Identify the blood parasite species.
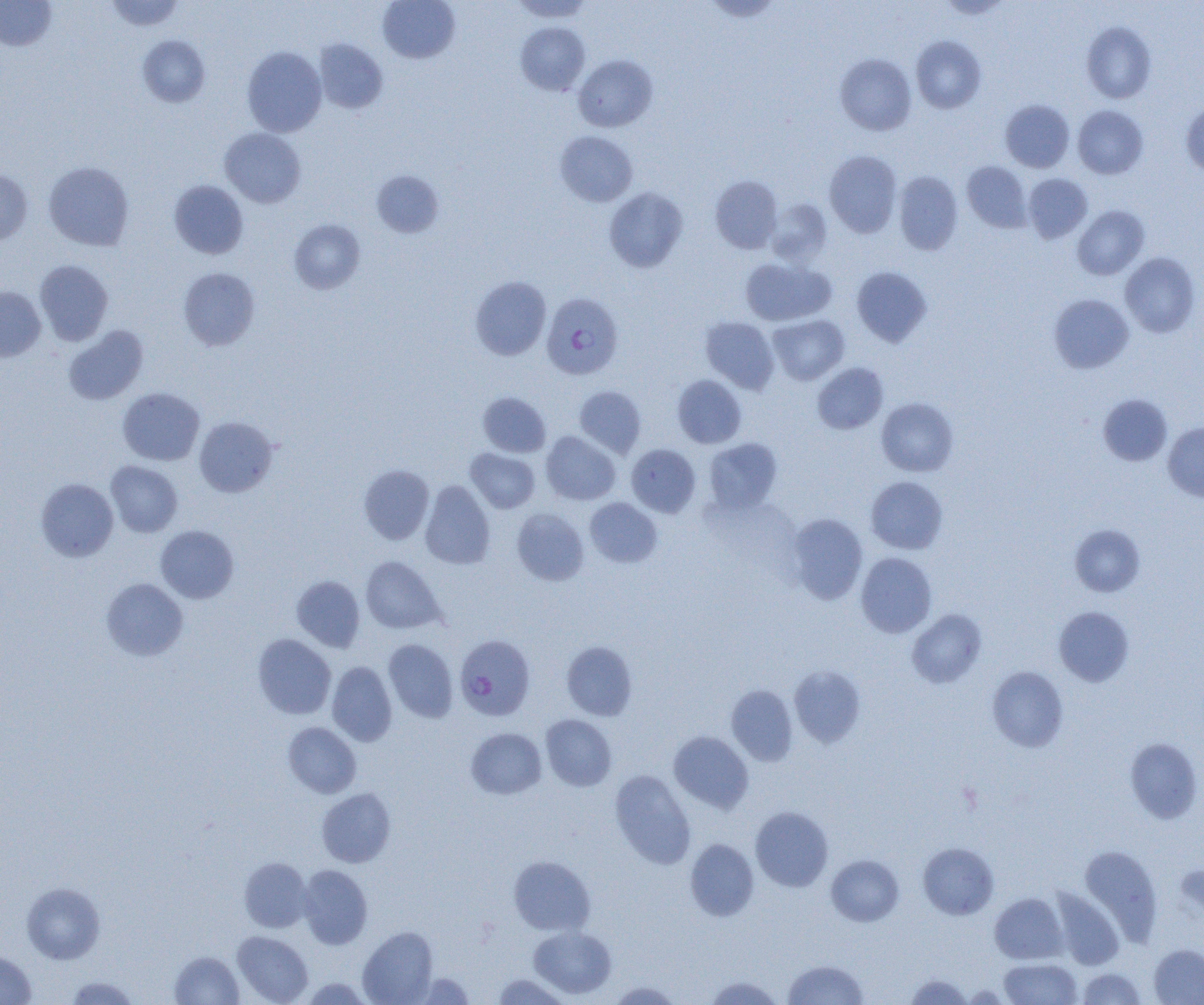

Plasmodium falciparum.

magnification = 1000x
Plasmodium falciparum-infected red blood cell locations = approximate bounding boxes as named x1/y1/x2/y2 corners in pixels: (x1=542, y1=292, x2=623, y2=379), (x1=455, y1=635, x2=535, y2=721)
preparation = thin blood smear
field of view = one of a larger specimen
modality = optical microscopy
image size = 1204×1005 pixels
uninfected red blood cell locations = approximate bounding boxes as named x1/y1/x2/y2 corners in pixels: (x1=0, y1=0, x2=56, y2=51), (x1=105, y1=0, x2=185, y2=31), (x1=378, y1=0, x2=460, y2=63), (x1=509, y1=0, x2=595, y2=22), (x1=938, y1=0, x2=1012, y2=19), (x1=1081, y1=21, x2=1156, y2=103), (x1=515, y1=22, x2=590, y2=95), (x1=138, y1=35, x2=210, y2=107), (x1=911, y1=35, x2=986, y2=114), (x1=314, y1=39, x2=388, y2=114), (x1=242, y1=46, x2=327, y2=137), (x1=835, y1=53, x2=916, y2=136), (x1=573, y1=54, x2=658, y2=132), (x1=1000, y1=99, x2=1074, y2=172), (x1=1181, y1=101, x2=1204, y2=177), (x1=1073, y1=105, x2=1148, y2=179), (x1=219, y1=127, x2=306, y2=208), (x1=555, y1=131, x2=638, y2=207), (x1=824, y1=150, x2=902, y2=237), (x1=962, y1=161, x2=1031, y2=233), (x1=43, y1=162, x2=134, y2=251), (x1=0, y1=169, x2=33, y2=245), (x1=372, y1=170, x2=444, y2=238), (x1=894, y1=171, x2=963, y2=255), (x1=1023, y1=173, x2=1093, y2=243), (x1=710, y1=175, x2=783, y2=253), (x1=169, y1=180, x2=248, y2=259), (x1=604, y1=187, x2=687, y2=272), (x1=766, y1=199, x2=832, y2=267), (x1=1072, y1=205, x2=1150, y2=280), (x1=289, y1=219, x2=365, y2=294), (x1=1120, y1=252, x2=1201, y2=337), (x1=740, y1=257, x2=834, y2=326), (x1=34, y1=260, x2=113, y2=345), (x1=852, y1=267, x2=932, y2=346), (x1=178, y1=268, x2=260, y2=350), (x1=470, y1=276, x2=551, y2=361), (x1=0, y1=286, x2=46, y2=361), (x1=1048, y1=293, x2=1134, y2=373), (x1=768, y1=315, x2=849, y2=385), (x1=701, y1=317, x2=779, y2=394), (x1=63, y1=326, x2=148, y2=405), (x1=812, y1=362, x2=888, y2=434), (x1=672, y1=375, x2=746, y2=448), (x1=574, y1=385, x2=646, y2=458), (x1=117, y1=388, x2=205, y2=466), (x1=478, y1=392, x2=551, y2=457), (x1=1098, y1=394, x2=1173, y2=466), (x1=876, y1=397, x2=959, y2=477), (x1=194, y1=416, x2=278, y2=497), (x1=1162, y1=422, x2=1204, y2=502), (x1=541, y1=431, x2=620, y2=505), (x1=704, y1=438, x2=782, y2=514), (x1=626, y1=444, x2=700, y2=517), (x1=465, y1=448, x2=539, y2=513), (x1=106, y1=461, x2=183, y2=537), (x1=358, y1=465, x2=434, y2=544), (x1=866, y1=476, x2=947, y2=554), (x1=36, y1=478, x2=118, y2=561), (x1=420, y1=480, x2=495, y2=569), (x1=585, y1=498, x2=662, y2=568), (x1=512, y1=508, x2=589, y2=586), (x1=786, y1=513, x2=868, y2=604), (x1=1070, y1=524, x2=1145, y2=596), (x1=155, y1=525, x2=239, y2=604), (x1=855, y1=552, x2=937, y2=638), (x1=360, y1=556, x2=445, y2=634), (x1=292, y1=575, x2=365, y2=652), (x1=101, y1=577, x2=188, y2=661), (x1=1054, y1=606, x2=1134, y2=686), (x1=906, y1=609, x2=987, y2=688), (x1=252, y1=634, x2=336, y2=719), (x1=383, y1=639, x2=458, y2=723), (x1=561, y1=641, x2=637, y2=721), (x1=327, y1=661, x2=397, y2=746), (x1=788, y1=665, x2=866, y2=748), (x1=987, y1=666, x2=1068, y2=752), (x1=726, y1=684, x2=797, y2=765), (x1=540, y1=714, x2=617, y2=791), (x1=283, y1=722, x2=361, y2=798), (x1=466, y1=727, x2=546, y2=799), (x1=668, y1=731, x2=754, y2=813), (x1=1125, y1=738, x2=1202, y2=823), (x1=609, y1=770, x2=696, y2=868), (x1=317, y1=788, x2=396, y2=867), (x1=750, y1=806, x2=834, y2=892), (x1=684, y1=838, x2=759, y2=921), (x1=918, y1=842, x2=998, y2=919), (x1=1080, y1=845, x2=1162, y2=945), (x1=508, y1=855, x2=596, y2=936), (x1=826, y1=855, x2=904, y2=926), (x1=239, y1=858, x2=312, y2=933), (x1=297, y1=864, x2=373, y2=949), (x1=22, y1=882, x2=105, y2=964), (x1=1051, y1=889, x2=1123, y2=969), (x1=989, y1=893, x2=1068, y2=964), (x1=529, y1=926, x2=616, y2=999), (x1=357, y1=927, x2=438, y2=1004), (x1=232, y1=931, x2=313, y2=1004), (x1=1149, y1=944, x2=1204, y2=1004), (x1=0, y1=950, x2=36, y2=1005), (x1=169, y1=950, x2=244, y2=1004), (x1=998, y1=958, x2=1082, y2=1004), (x1=783, y1=959, x2=869, y2=1004), (x1=1076, y1=968, x2=1146, y2=1004), (x1=411, y1=972, x2=475, y2=1004), (x1=905, y1=973, x2=973, y2=1004), (x1=492, y1=974, x2=570, y2=1004), (x1=65, y1=975, x2=142, y2=1005), (x1=704, y1=975, x2=784, y2=1005), (x1=300, y1=977, x2=372, y2=1004), (x1=608, y1=981, x2=684, y2=1004)